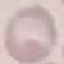

Result: no malaria parasites seen. Cell patch, automatically extracted from a larger field of view and resized to 64 × 64 pixels. Acquired by smartphone through the microscope eyepiece. Thin blood film. Giemsa stain.